Identify the parasite.
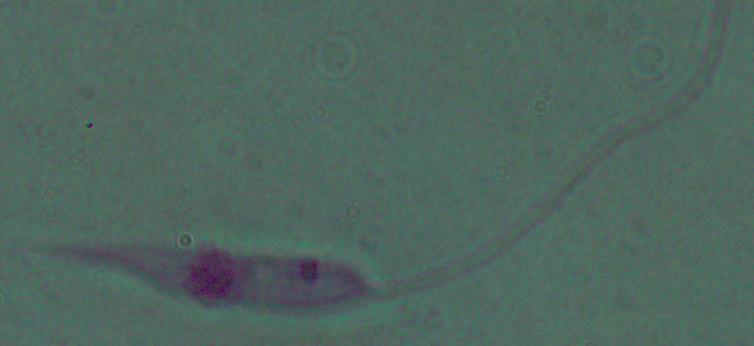

This is Leishmania.

modality = micrograph
magnification = 1000x